State which parasite is depicted.
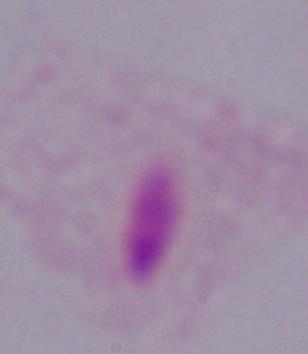

This is a trichomonad.

{
  "magnification": "1000x",
  "modality": "micrograph"
}